Name the parasite shown.
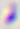
Toxoplasma gondii.

modality = micrograph
magnification = 400x